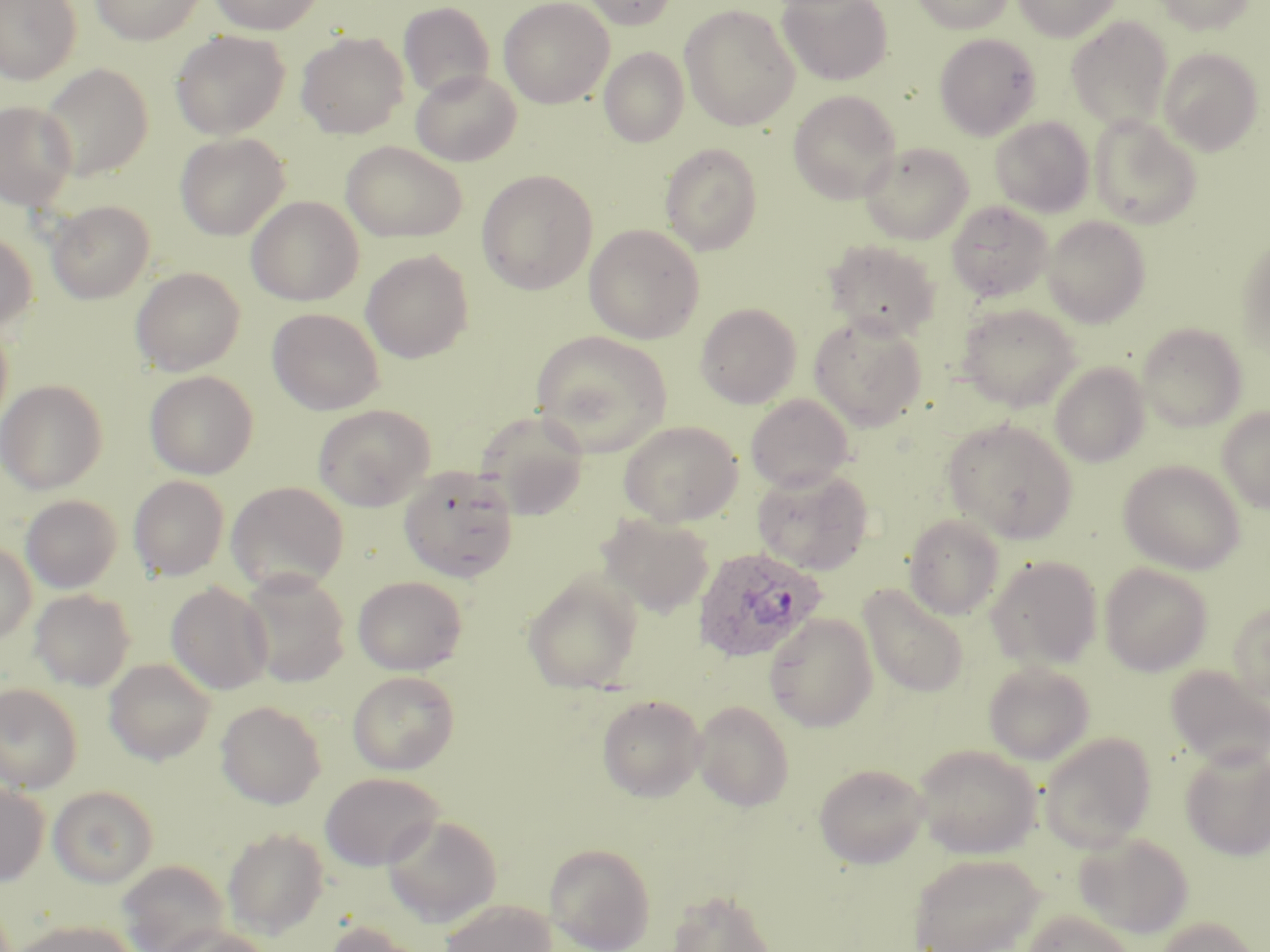
Approximate bounding boxes as (x1,y1)-(x2,y2) corner pairs in pixels. Plasmodium ovale-infected red blood cell locations: (692,546)-(826,663). Uninfected red blood cell locations: (0,0)-(82,84), (89,0)-(207,44), (207,0)-(325,35), (498,0)-(614,108), (579,0)-(679,30), (910,0)-(1014,34), (1012,0)-(1121,41), (1153,0)-(1257,34), (778,1)-(894,86), (398,2)-(495,102), (680,4)-(800,131), (1066,16)-(1172,131), (170,30)-(290,140), (296,31)-(409,139), (934,32)-(1041,140), (599,47)-(689,148), (1159,47)-(1265,155), (38,63)-(152,179), (410,68)-(521,167), (788,90)-(901,203), (0,100)-(78,212), (1089,115)-(1201,229), (990,116)-(1094,216), (175,133)-(289,240), (340,141)-(468,242), (859,141)-(974,244), (660,143)-(762,255), (477,170)-(598,294), (246,196)-(364,306), (47,200)-(155,304), (946,200)-(1053,302), (1043,216)-(1151,327), (584,224)-(704,343), (0,231)-(37,335), (1236,238)-(1270,357), (824,239)-(941,341), (361,250)-(474,363), (130,266)-(245,375), (696,302)-(801,408), (957,302)-(1080,411), (267,307)-(384,415), (809,315)-(927,431), (0,322)-(13,435), (1137,322)-(1247,432), (531,331)-(672,456), (1050,362)-(1150,467), (144,370)-(258,479), (0,379)-(107,494), (745,394)-(854,493), (313,404)-(435,511), (1217,406)-(1270,513), (474,409)-(591,518), (943,418)-(1077,543), (619,420)-(743,527), (1118,460)-(1245,574), (398,465)-(519,584), (752,467)-(874,575), (129,475)-(230,581), (226,482)-(348,593), (21,494)-(122,593), (598,514)-(714,618), (904,514)-(1005,620), (0,542)-(37,645), (986,555)-(1102,670), (1099,563)-(1213,676), (237,569)-(350,687), (523,572)-(642,694), (352,575)-(467,674), (166,582)-(273,695), (859,584)-(969,697), (29,589)-(135,691), (1228,602)-(1270,703), (764,613)-(878,732), (104,658)-(216,765), (983,661)-(1095,765), (1165,665)-(1270,770), (347,671)-(459,774), (0,683)-(83,793), (597,694)-(707,802), (215,700)-(326,809), (692,700)-(794,813), (1038,731)-(1157,852), (913,743)-(1042,859), (1180,745)-(1270,861), (813,762)-(930,869), (320,772)-(445,871), (0,783)-(50,886), (49,785)-(158,888), (382,814)-(502,927), (222,828)-(329,938), (1073,832)-(1194,939), (545,842)-(656,952), (908,852)-(1045,952), (117,860)-(230,952), (667,888)-(778,952), (439,900)-(557,952), (1021,909)-(1135,952), (1152,916)-(1260,952), (13,919)-(138,952), (322,920)-(425,952), (155,926)-(276,952). Slide-level diagnosis: Plasmodium ovale. Image is 1270×952 pixels. Thin blood film. 1000x magnification. One field of a larger specimen. May-Grünwald-Giemsa-stained preparation. Optical microscopy.